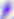
Summary:
  - Modality: photomicrograph
  - Magnification: 400x
  - Identification: Toxoplasma gondii